Identify the parasite.
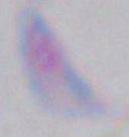

This is Toxoplasma gondii.

1000x magnification. Photomicrograph.